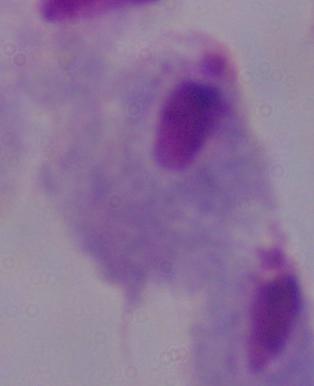
Micrograph. A trichomonad is seen. Captured at 1000x magnification.